Locate and identify every blood parasite.
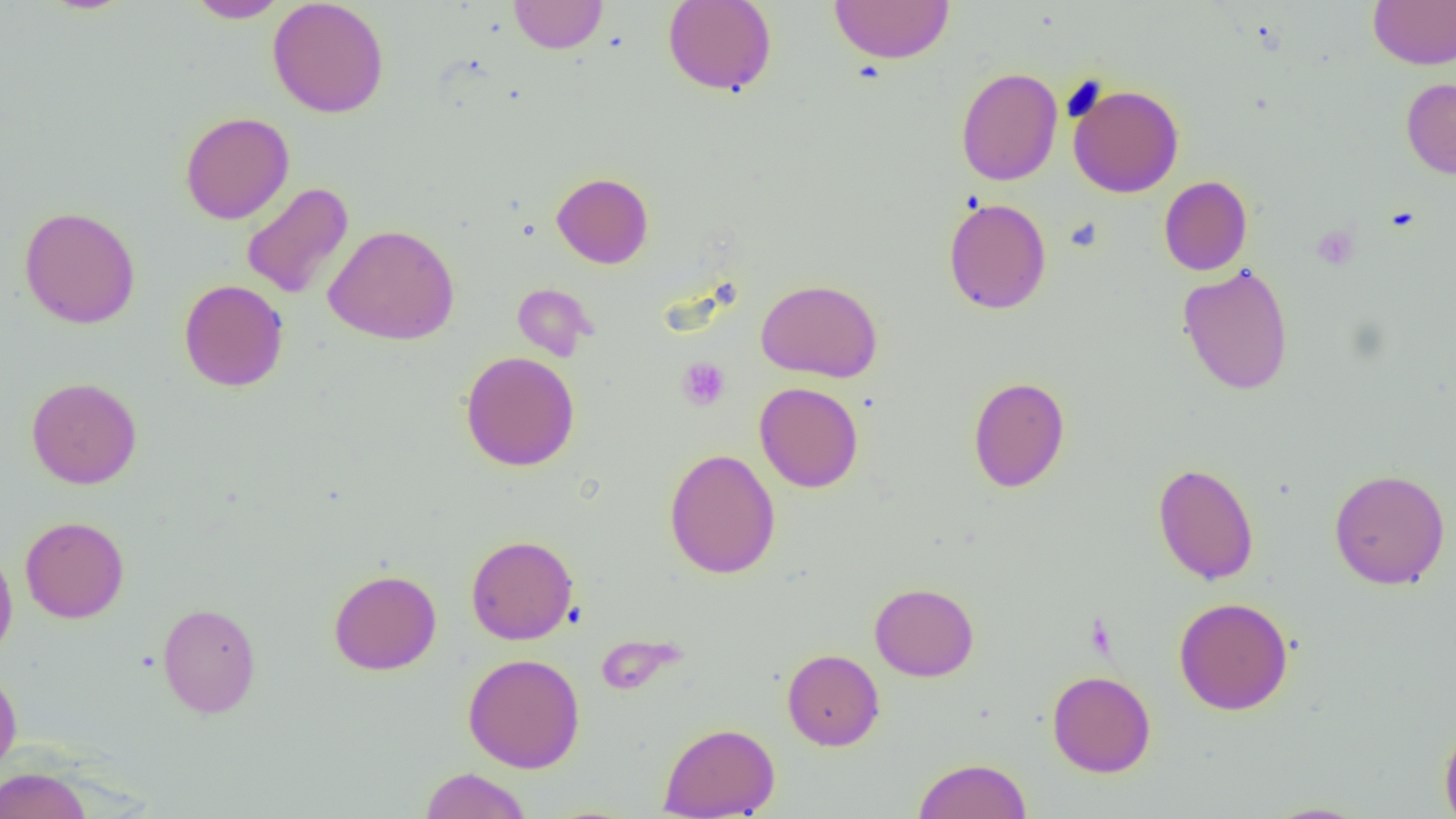

No blood parasites observed.

Summary:
  - Coordinate format: approximate bounding boxes as (x1,y1)-(x2,y2) corner pairs in pixels
  - Uninfected red blood cell locations: (185,0)-(289,22), (268,0)-(389,118), (508,0)-(608,54), (662,0)-(777,97), (1368,0)-(1456,69), (829,1)-(954,64), (956,67)-(1063,186), (1401,78)-(1456,178), (1068,83)-(1184,198), (180,111)-(293,224), (552,172)-(653,268), (1159,176)-(1252,276), (241,182)-(353,299), (943,197)-(1051,314), (19,206)-(140,329), (324,224)-(460,345), (1177,263)-(1294,395), (756,278)-(883,383), (179,279)-(289,392), (513,282)-(596,362), (460,351)-(580,471), (26,376)-(142,489), (968,376)-(1070,493), (754,382)-(864,493), (665,448)-(780,579), (1152,463)-(1259,585), (1329,469)-(1450,589), (20,515)-(129,623), (466,535)-(578,644), (0,542)-(18,663), (329,569)-(442,675), (869,583)-(979,682), (1174,597)-(1293,715), (157,602)-(261,718), (782,649)-(884,751), (462,653)-(585,773), (0,670)-(22,779), (1047,670)-(1156,777), (1439,720)-(1456,819), (659,722)-(779,818), (913,757)-(1032,818), (420,767)-(532,819), (0,768)-(92,819), (1260,801)-(1374,818)
  - Platelet locations: (1311,226)-(1359,269), (677,357)-(730,411)
  - Slide-level diagnosis: negative for blood parasites
  - Image size: 1456×819 pixels
  - Field of view: single
  - Modality: optical microscopy
  - Preparation: thin blood smear
  - Magnification: 1000x